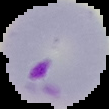

Summary:
  - Result: malaria parasites detected
  - Preparation: thin blood smear
  - Image size: 109×109 pixels
  - Image type: segmented cell region on a black background